State the preparation type.
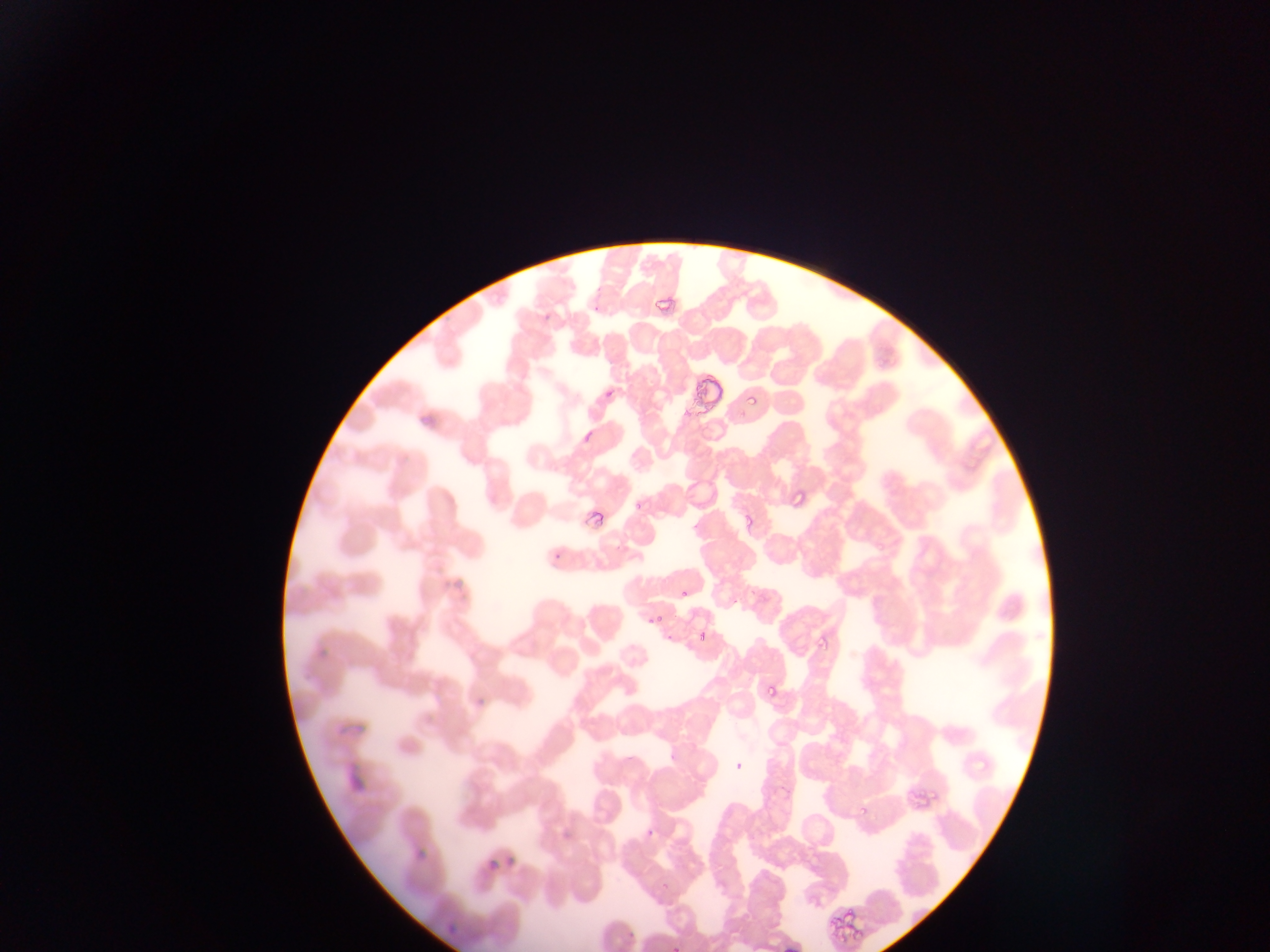
This is a thin smear.

Approximate bounding boxes as (left, top, right, bottom) in pixels.
Summary:
  - Plasmodium parasite locations: (652, 286, 681, 326), (543, 304, 557, 326), (604, 376, 626, 395), (743, 390, 763, 412), (580, 427, 594, 450), (790, 489, 805, 508), (632, 500, 644, 515), (584, 503, 608, 530), (740, 507, 759, 531), (553, 547, 562, 559), (676, 590, 688, 604), (643, 613, 662, 630), (694, 626, 706, 641), (818, 631, 832, 652), (763, 684, 780, 701), (857, 803, 874, 817), (644, 823, 659, 840), (845, 911, 858, 924), (829, 914, 841, 932), (838, 934, 857, 946), (666, 948, 680, 952)
  - Country: Ghana
  - Capture: mobile-phone photograph through a microscope
  - Image size: 1270×952 pixels
  - Field of view: single